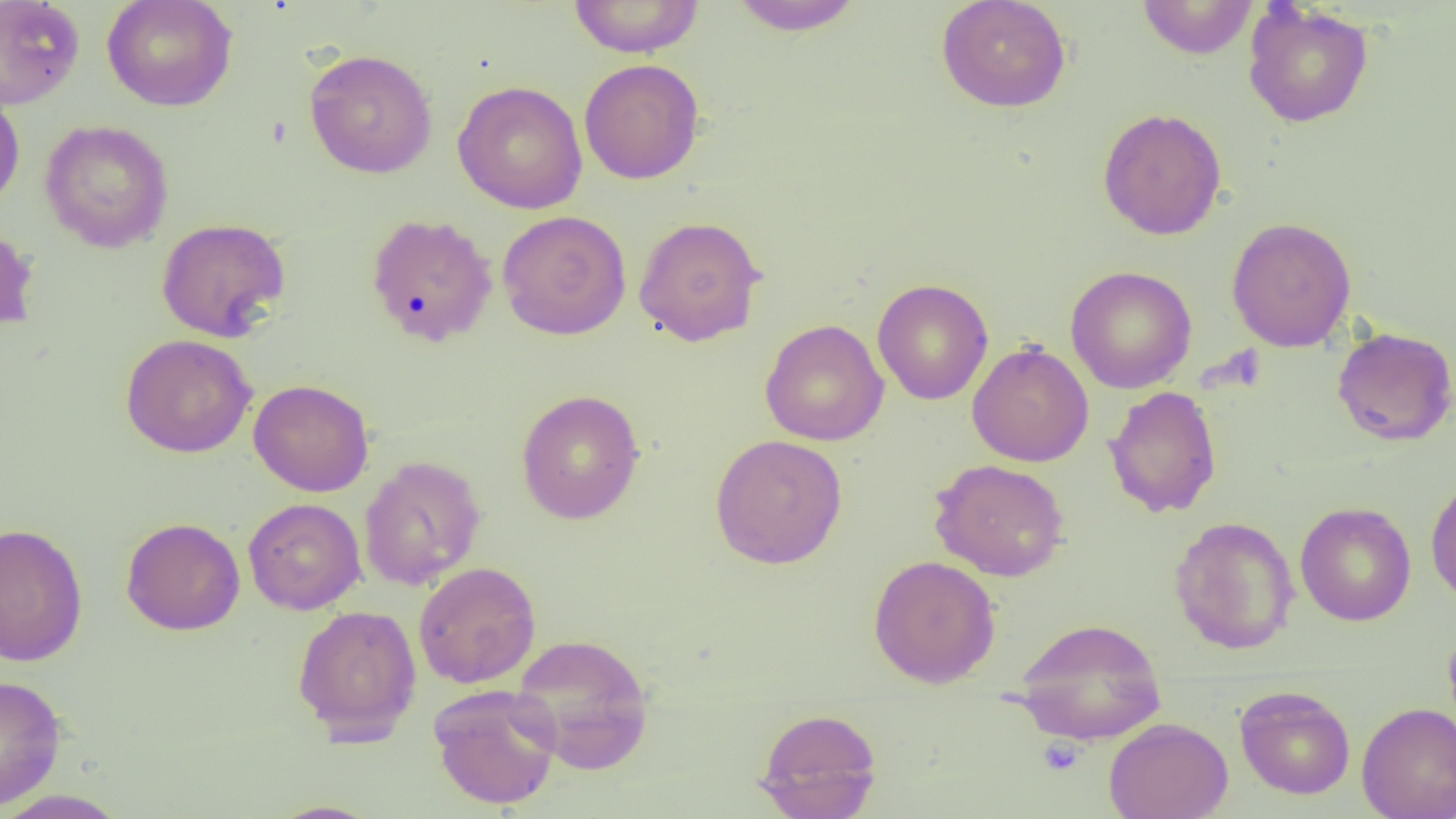
Summary:
  - Coordinate format: approximate bounding boxes as (x1,y1)-(x2,y2) corner pairs in pixels
  - Platelet locations: (1038,736)-(1085,776)
  - Uninfected red blood cell locations: (0,0)-(85,110), (102,0)-(238,111), (568,0)-(705,58), (728,0)-(864,36), (936,0)-(1071,113), (1137,1)-(1258,59), (1242,3)-(1374,128), (304,48)-(438,178), (578,58)-(705,184), (452,80)-(588,214), (0,86)-(25,214), (1097,108)-(1227,240), (40,119)-(174,253), (497,210)-(631,340), (365,213)-(498,347), (633,215)-(767,346), (1226,217)-(1357,352), (156,218)-(291,342), (0,222)-(39,335), (1065,265)-(1197,394), (872,279)-(993,405), (760,319)-(889,446), (1331,327)-(1456,446), (120,334)-(257,458), (967,341)-(1094,467), (249,379)-(374,497), (1104,386)-(1222,518), (516,389)-(645,525), (710,434)-(848,569), (358,456)-(486,591), (929,458)-(1070,581), (1425,474)-(1456,606), (243,497)-(366,615), (1295,502)-(1416,626), (1169,515)-(1299,655), (120,517)-(245,636), (0,522)-(88,666), (868,554)-(1001,688), (413,561)-(541,688), (292,604)-(423,742), (1012,618)-(1166,742), (1442,625)-(1456,737), (510,633)-(655,774), (0,675)-(66,809), (428,684)-(562,810), (1234,685)-(1355,800), (1356,702)-(1456,818), (755,707)-(883,818), (1104,717)-(1233,819), (0,789)-(130,818), (264,799)-(384,818)
  - Slide-level diagnosis: no evidence of blood parasites
  - Image size: 1456×819 pixels
  - Magnification: 1000x
  - Modality: light microscopy
  - Field of view: single
  - Preparation: thin blood film